Give the position of every Plasmodium parasite.
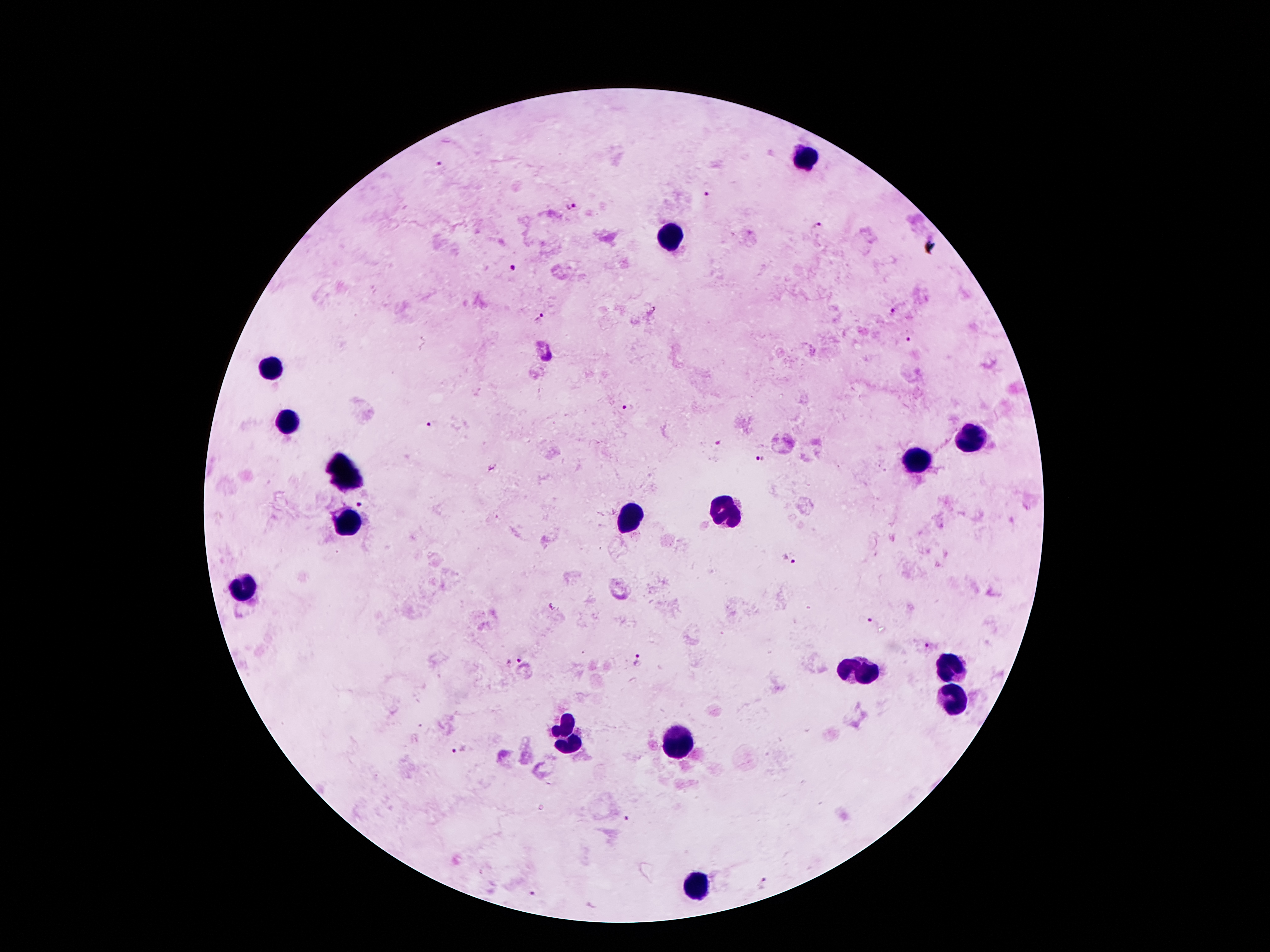

Approximate centers as (x, y) in pixels.
Plasmodium parasites: (439, 163), (707, 193), (569, 205), (817, 227), (513, 270), (893, 310), (540, 316), (908, 340), (626, 408), (434, 424), (716, 443), (761, 459), (360, 505), (789, 560), (868, 621), (928, 645), (521, 658), (639, 660), (456, 751), (627, 817), (763, 882), (534, 892).

Summary:
  - Leukocyte locations: (807, 157), (671, 239), (271, 369), (287, 421), (965, 439), (915, 461), (345, 475), (729, 513), (627, 519), (351, 521), (243, 587), (861, 671), (951, 671), (953, 701), (565, 735), (679, 741), (695, 887)
  - Capture: smartphone through the microscope eyepiece
  - Image size: 1270×952 pixels
  - Stain: Giemsa
  - Patient malaria status: infected with Plasmodium falciparum
  - Field of view: single
  - Preparation: thick blood film
  - Magnification: 100x